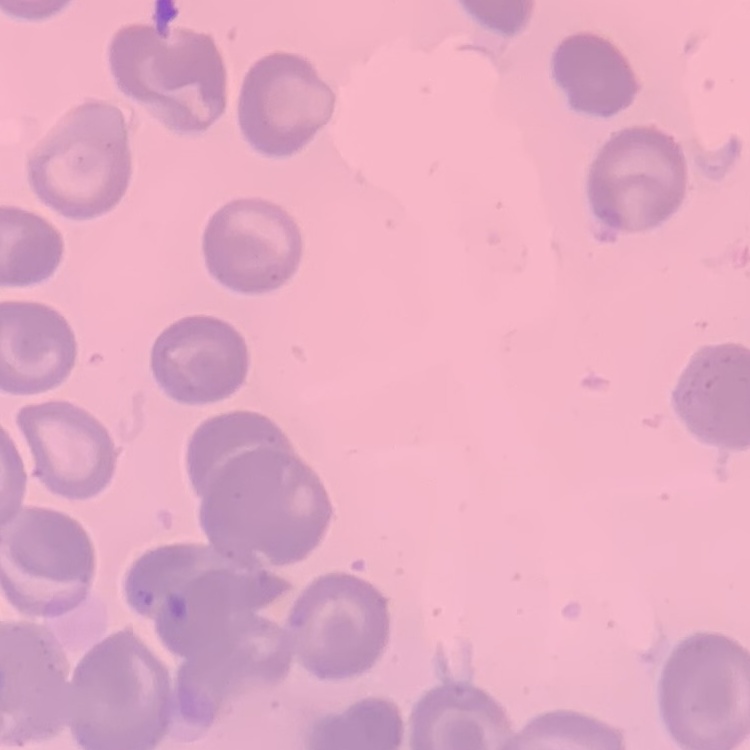
Summary:
  - Erythrocyte morphology: no rouleaux formation
  - Preparation: thin blood film
  - Stain: Field's or Giemsa
  - Image type: one tile cut from a larger photomicrograph